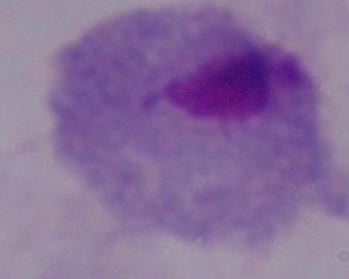
{
  "magnification": "1000x",
  "identification": "trichomonad",
  "modality": "photomicrograph"
}